Describe the morphology of the erythrocytes.
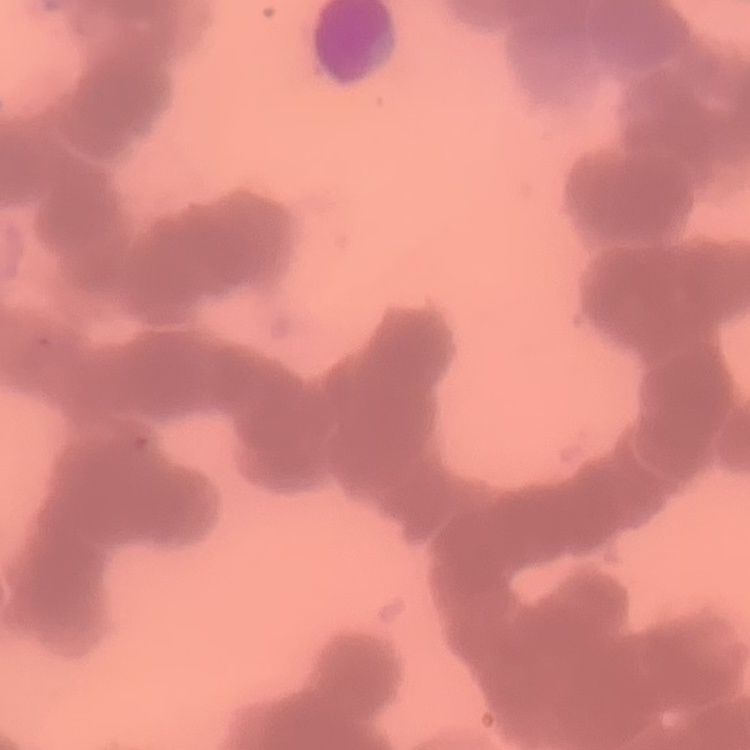

They show rouleaux formation.

One tile cut from a larger photomicrograph. Stained with either Field's or Giemsa. Thin blood smear.